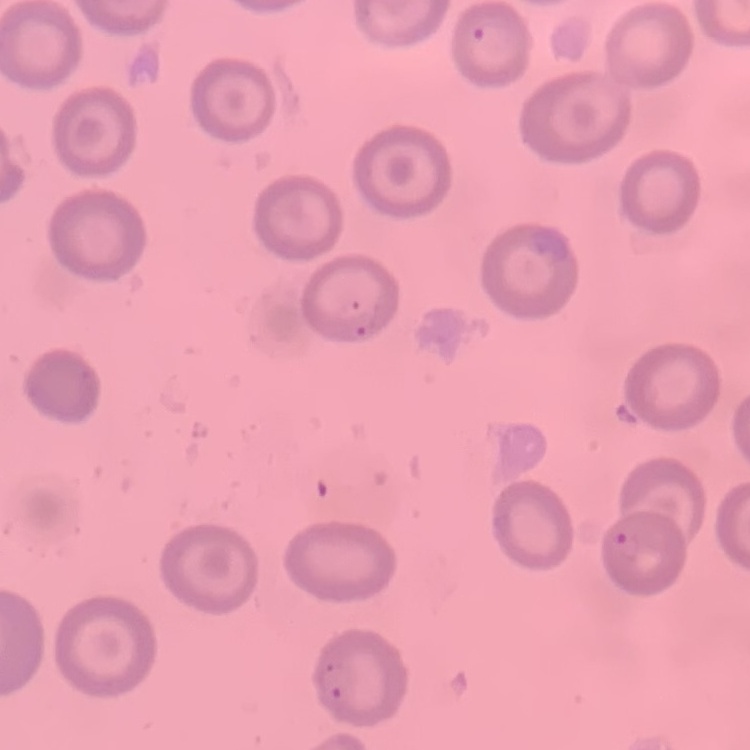

red_blood_cell_morphology: no rouleaux formation
preparation: thin blood smear
stain: Field's or Giemsa
image_type: one tile cut from a larger photomicrograph